Locate every Plasmodium falciparum-infected red blood cell.
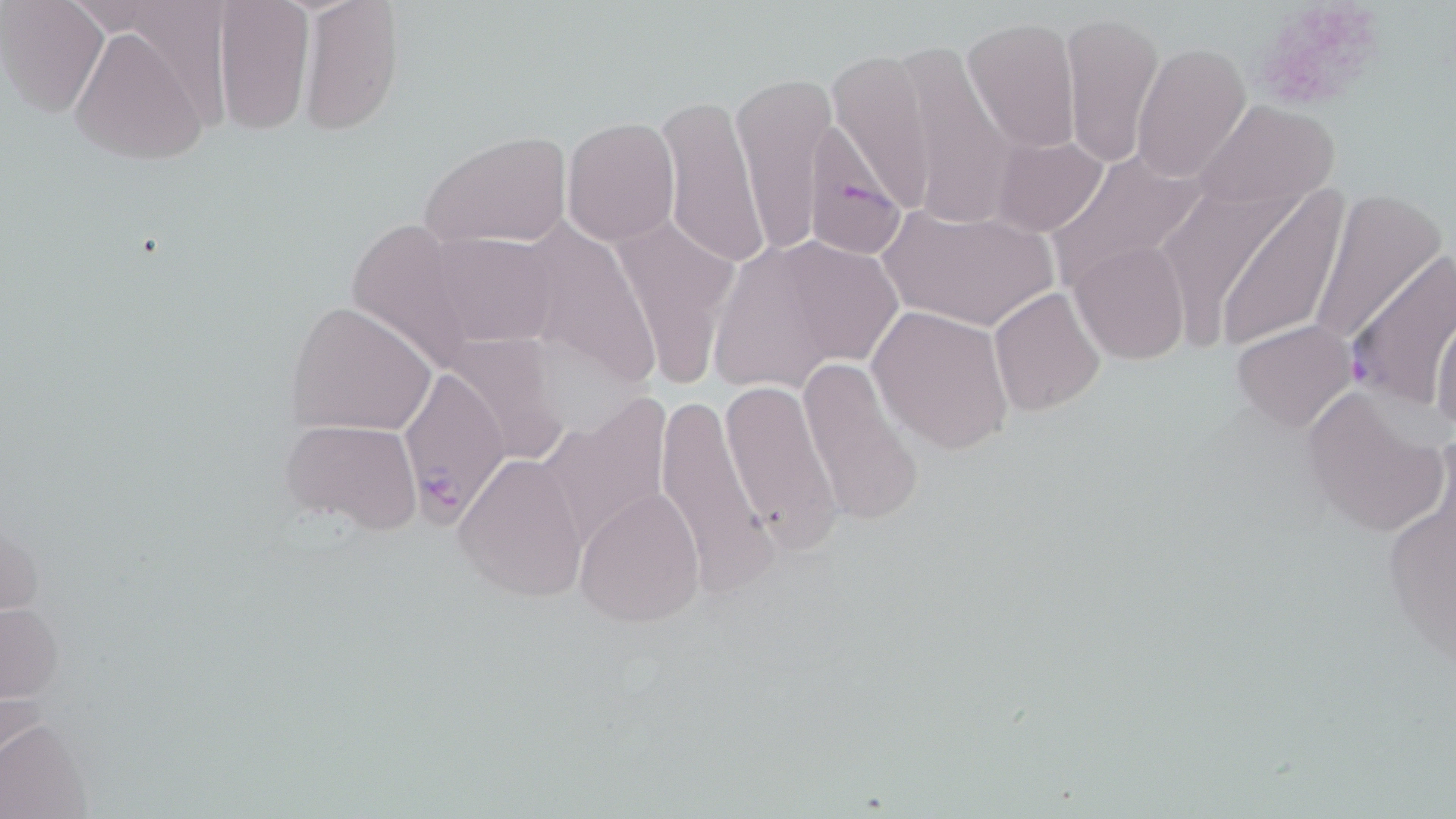
Approximate bounding boxes as named x1/y1/x2/y2 corners in pixels.
Plasmodium falciparum-infected red blood cells: (x1=803, y1=118, x2=916, y2=265), (x1=1346, y1=250, x2=1455, y2=410), (x1=400, y1=365, x2=508, y2=527).

Summary:
  - Platelet locations: (x1=1258, y1=7, x2=1377, y2=114)
  - Uninfected red blood cell locations: (x1=211, y1=0, x2=316, y2=135), (x1=297, y1=0, x2=406, y2=137), (x1=0, y1=2, x2=108, y2=115), (x1=1061, y1=10, x2=1164, y2=172), (x1=961, y1=15, x2=1081, y2=152), (x1=67, y1=23, x2=211, y2=167), (x1=1131, y1=41, x2=1251, y2=181), (x1=827, y1=49, x2=936, y2=216), (x1=730, y1=75, x2=833, y2=255), (x1=658, y1=94, x2=766, y2=273), (x1=1190, y1=98, x2=1341, y2=218), (x1=562, y1=117, x2=679, y2=247), (x1=421, y1=132, x2=573, y2=248), (x1=987, y1=136, x2=1109, y2=238), (x1=1043, y1=146, x2=1208, y2=289), (x1=1146, y1=174, x2=1307, y2=346), (x1=1215, y1=185, x2=1349, y2=355), (x1=1305, y1=188, x2=1446, y2=353), (x1=876, y1=203, x2=1061, y2=332), (x1=611, y1=213, x2=739, y2=391), (x1=426, y1=231, x2=561, y2=348), (x1=1070, y1=240, x2=1189, y2=365), (x1=706, y1=245, x2=849, y2=394), (x1=988, y1=288, x2=1106, y2=414), (x1=285, y1=299, x2=439, y2=437), (x1=868, y1=304, x2=1014, y2=454), (x1=1431, y1=311, x2=1456, y2=442), (x1=1231, y1=320, x2=1358, y2=432), (x1=446, y1=331, x2=574, y2=466), (x1=798, y1=355, x2=924, y2=529), (x1=720, y1=380, x2=842, y2=549), (x1=1299, y1=384, x2=1448, y2=539), (x1=652, y1=393, x2=774, y2=594), (x1=281, y1=418, x2=424, y2=535), (x1=1377, y1=452, x2=1455, y2=680), (x1=453, y1=454, x2=589, y2=603), (x1=575, y1=487, x2=706, y2=627), (x1=0, y1=602, x2=62, y2=699), (x1=0, y1=718, x2=93, y2=819)
  - Slide-level diagnosis: Plasmodium falciparum
  - Image size: 1456×819 pixels
  - Preparation: thin blood film
  - Field of view: one of a larger specimen
  - Magnification: 1000x
  - Modality: light microscopy
  - Stain: May-Grünwald-Giemsa